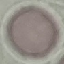
malaria status = uninfected
stain = Giemsa
capture = smartphone through the microscope eyepiece
image type = automatically extracted cell patch, resized to 64 × 64 pixels
preparation = thin smear